Assess the morphology of the red blood cells.
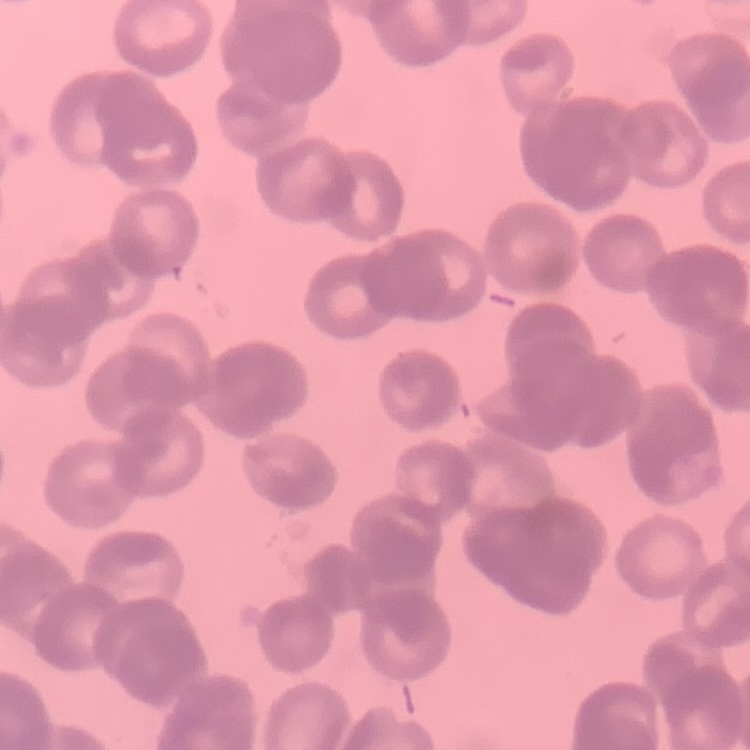
They show rouleaux formation.

stain = Field's or Giemsa
image type = square crop of a larger photomicrograph
preparation = thin blood smear